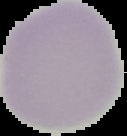
{
  "image_size": "127×136 pixels",
  "result": "no Plasmodium parasites seen",
  "preparation": "thin blood smear",
  "image_type": "cell region segmented out of the field of view; surrounding area masked to black"
}